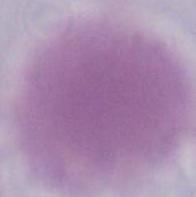 1000x magnification. Photomicrograph. A red blood cell is seen.